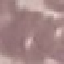
result = no malaria parasites detected
stain = Giemsa
capture = smartphone camera at the microscope eyepiece
preparation = thin blood film
image type = cell patch, automatically extracted from a larger field of view and resized to 64 × 64 pixels